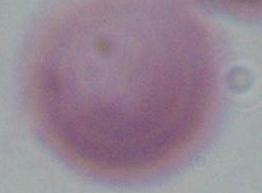

Summary:
  - Modality: micrograph
  - Identification: red blood cell
  - Magnification: 1000x